Point out each Plasmodium parasite and each leukocyte.
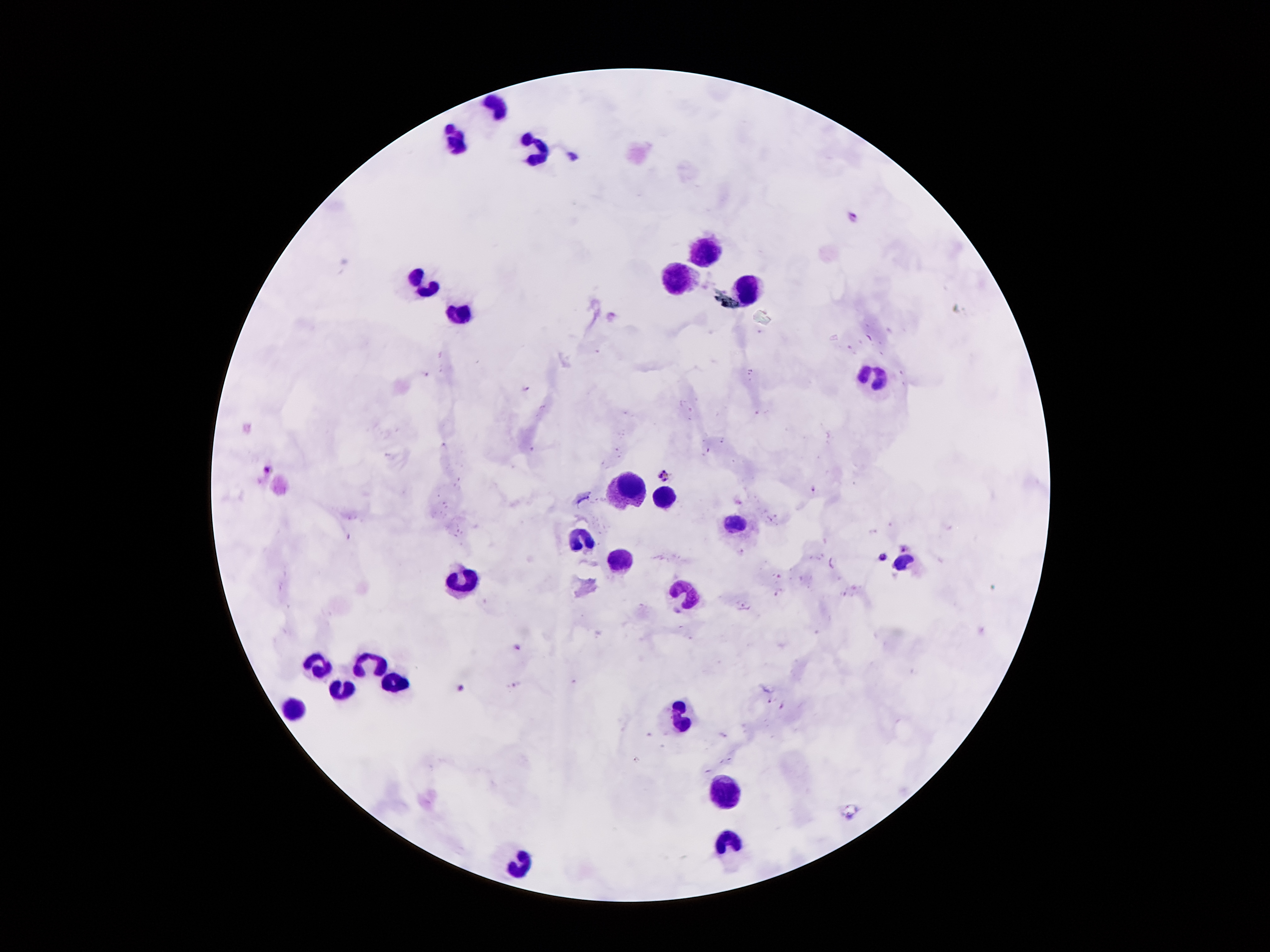

Approximate centers as [x, y] in pixels.
Plasmodium parasites: [574, 158], [854, 212], [610, 315], [426, 374], [525, 389], [269, 470], [663, 474], [814, 490], [905, 546], [881, 555], [518, 645], [463, 688], [770, 702].
Leukocytes: [498, 106], [455, 140], [532, 149], [698, 249], [419, 283], [680, 283], [750, 288], [460, 313], [873, 378], [630, 490], [664, 501], [734, 521], [578, 540], [616, 560], [900, 562], [460, 583], [687, 592], [366, 660], [316, 664], [396, 685], [339, 689], [296, 707], [684, 710], [725, 794], [730, 844], [516, 866].

Patient malaria status: positive for Plasmodium falciparum. 100x magnification. Smartphone photograph taken through the microscope eyepiece. Thick blood smear. Image is 1270×952 pixels. One field from this slide. Giemsa stain.